Assess the morphology of the erythrocytes.
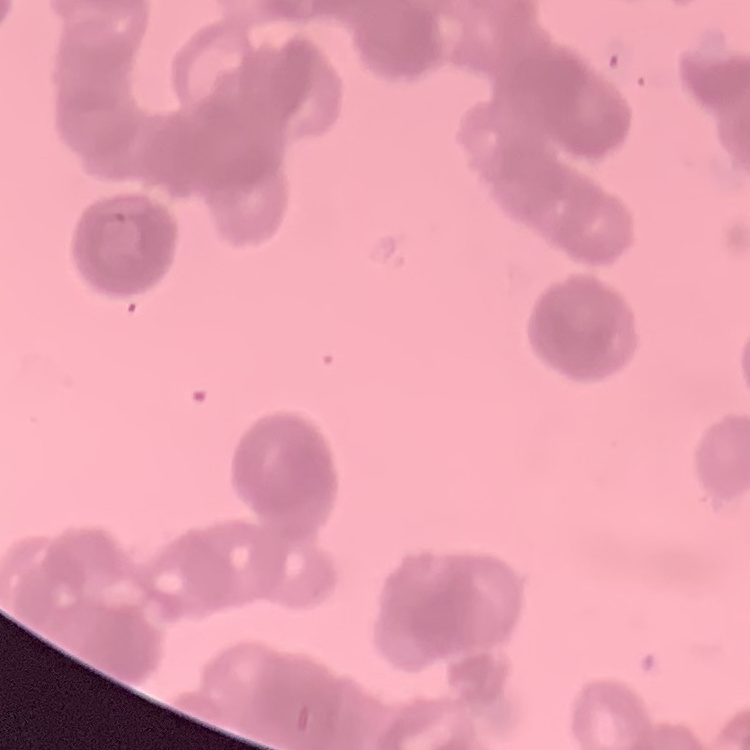
They show rouleaux formation.

One tile cut from a larger photomicrograph. Field's or Giemsa stain. Thin blood film.